Give the preparation type.
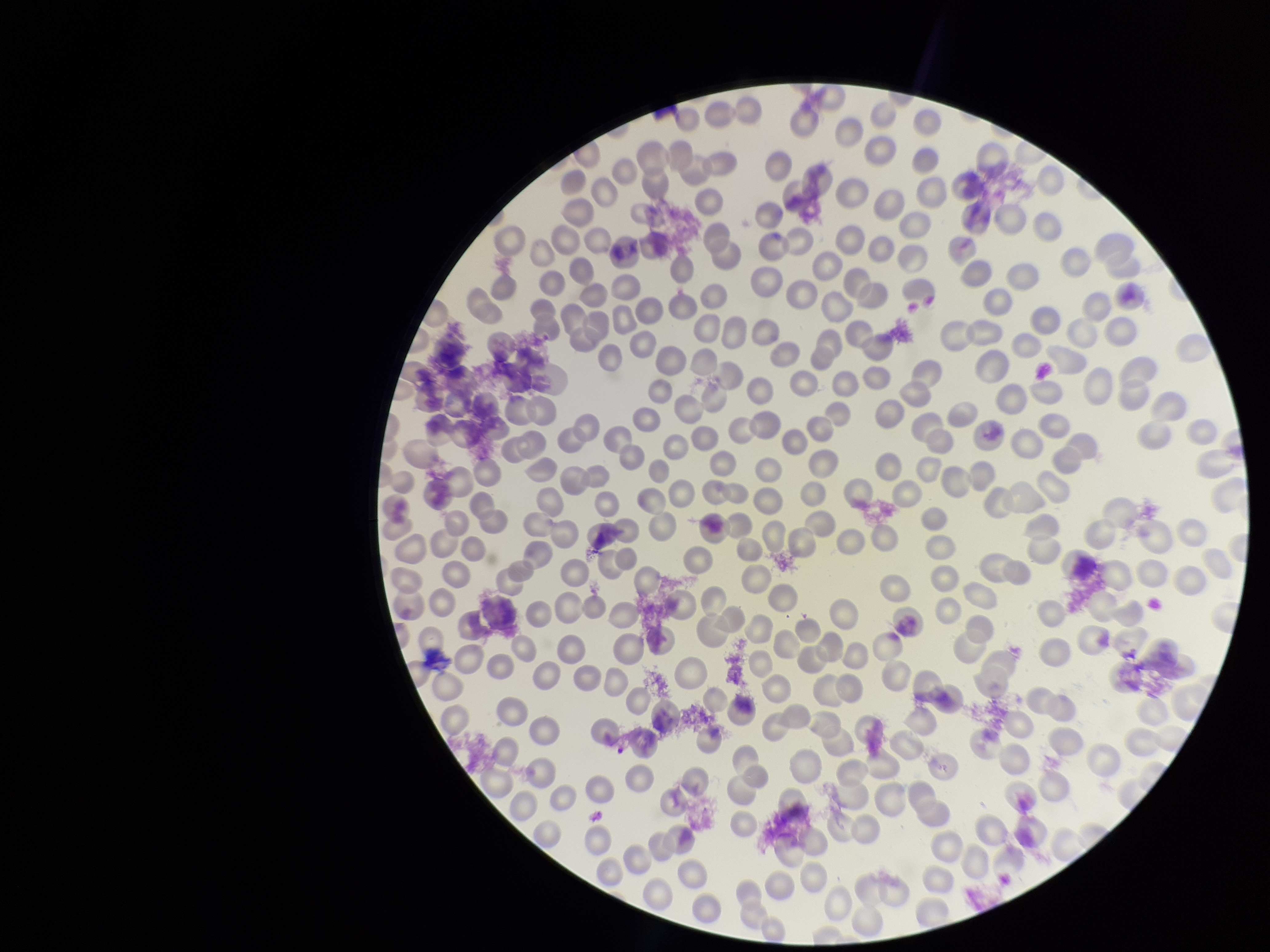
It is a thin blood smear.

Parasitized red blood cell count: 0. Red blood cell count: 247. Patient malaria status: negative. Parasitized red blood cells: none detected. Giemsa stain. Smartphone photograph taken through the eyepiece of a microscope. Image is 1270×952 pixels. One field from this slide.